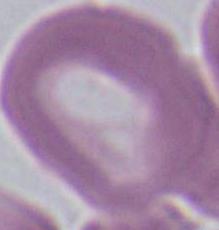
Micrograph. Captured at 1000x magnification. A red blood cell is seen.